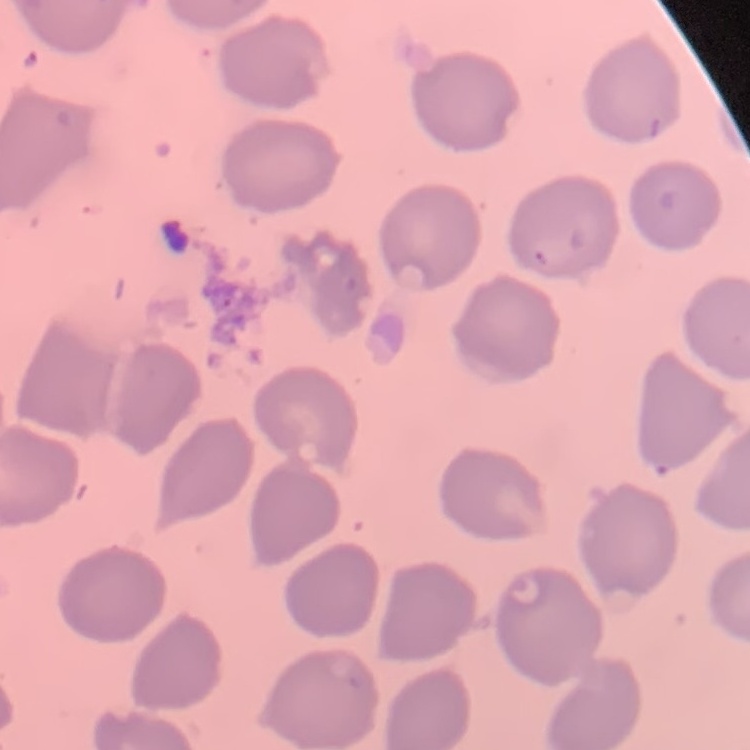

The red blood cells exhibit no rouleaux formation. Field's or Giemsa stain. Square crop of a larger photomicrograph. Thin peripheral smear.